Report the malaria status of this cell.
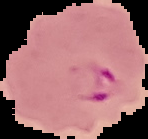

It is parasitized.

Summary:
  - Preparation: thin blood film
  - Image size: 148×139 pixels
  - Image type: cell region segmented out of the field of view; surrounding area masked to black